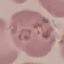
Summary:
  - Result: malaria parasites detected
  - Preparation: thin smear
  - Stain: Giemsa
  - Image type: cell patch, automatically extracted from a larger field of view and resized to 64 × 64 pixels
  - Capture: smartphone through the microscope eyepiece